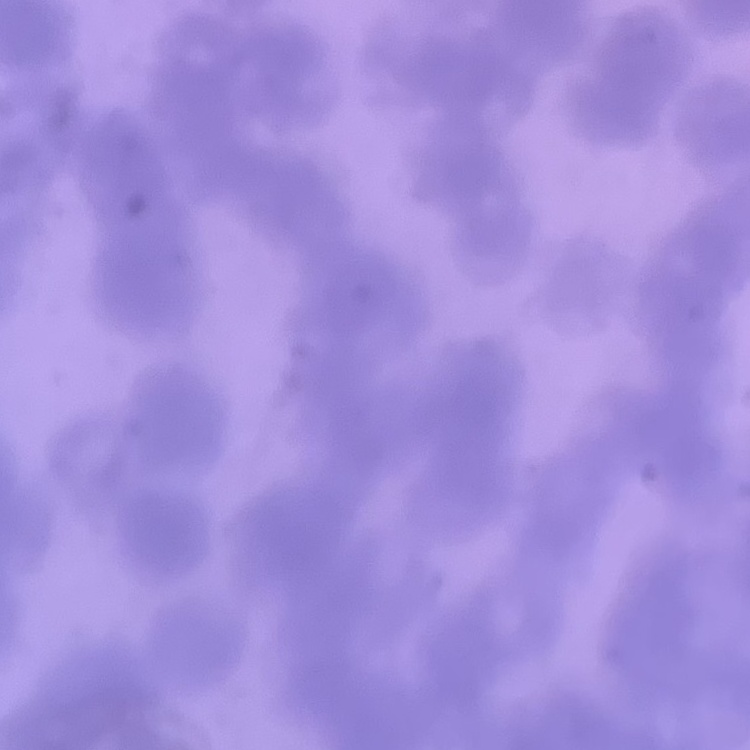

{
  "erythrocyte_morphology": "rouleaux formation",
  "image_type": "square crop of a larger photomicrograph",
  "stain": "Field's or Giemsa",
  "preparation": "thin peripheral smear"
}